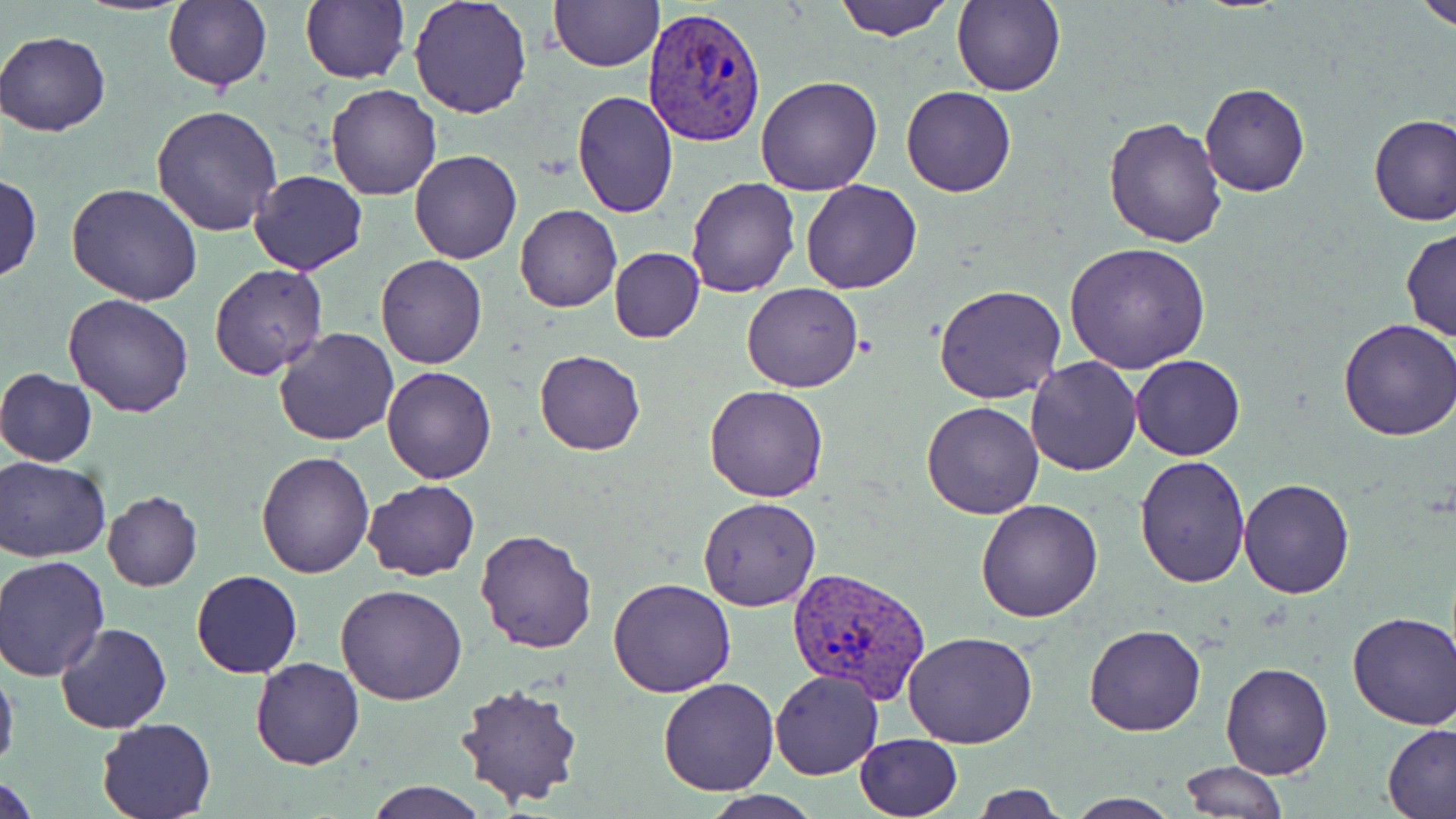

{
  "slide_level_diagnosis": "Plasmodium vivax",
  "stain": "May-Grünwald-Giemsa",
  "image_size": "1456×819 pixels",
  "field_of_view": "single",
  "preparation": "thin blood film",
  "plasmodium_vivax_infected_red_blood_cell_locations": "approximate bounding boxes as named x1/y1/x2/y2 corners in pixels: (x1=641, y1=6, x2=767, y2=149), (x1=788, y1=565, x2=931, y2=704)",
  "uninfected_red_blood_cell_locations": "approximate bounding boxes as named x1/y1/x2/y2 corners in pixels: (x1=74, y1=0, x2=194, y2=14), (x1=300, y1=0, x2=410, y2=84), (x1=407, y1=0, x2=533, y2=119), (x1=833, y1=0, x2=953, y2=42), (x1=952, y1=0, x2=1066, y2=98), (x1=1416, y1=0, x2=1456, y2=33), (x1=163, y1=1, x2=272, y2=92), (x1=548, y1=1, x2=662, y2=71), (x1=1, y1=29, x2=111, y2=137), (x1=755, y1=74, x2=883, y2=197), (x1=326, y1=83, x2=442, y2=201), (x1=1199, y1=83, x2=1311, y2=198), (x1=901, y1=87, x2=1017, y2=196), (x1=572, y1=90, x2=679, y2=217), (x1=149, y1=103, x2=283, y2=237), (x1=1367, y1=113, x2=1456, y2=227), (x1=1103, y1=115, x2=1229, y2=248), (x1=409, y1=148, x2=522, y2=265), (x1=248, y1=170, x2=368, y2=276), (x1=0, y1=173, x2=43, y2=283), (x1=684, y1=176, x2=800, y2=298), (x1=800, y1=178, x2=923, y2=294), (x1=66, y1=182, x2=203, y2=306), (x1=515, y1=205, x2=622, y2=312), (x1=1400, y1=228, x2=1455, y2=342), (x1=1064, y1=241, x2=1211, y2=374), (x1=609, y1=247, x2=705, y2=344), (x1=376, y1=255, x2=487, y2=369), (x1=208, y1=265, x2=329, y2=381), (x1=741, y1=280, x2=863, y2=393), (x1=935, y1=283, x2=1067, y2=405), (x1=63, y1=293, x2=194, y2=419), (x1=1334, y1=318, x2=1456, y2=440), (x1=273, y1=326, x2=401, y2=446), (x1=534, y1=349, x2=646, y2=455), (x1=1130, y1=354, x2=1244, y2=460), (x1=1026, y1=356, x2=1141, y2=475), (x1=382, y1=366, x2=497, y2=484), (x1=0, y1=368, x2=98, y2=466), (x1=705, y1=385, x2=829, y2=503), (x1=920, y1=401, x2=1046, y2=520), (x1=256, y1=450, x2=374, y2=578), (x1=0, y1=456, x2=110, y2=562), (x1=1134, y1=456, x2=1252, y2=589), (x1=1238, y1=478, x2=1355, y2=599), (x1=361, y1=480, x2=481, y2=580), (x1=102, y1=489, x2=202, y2=592), (x1=697, y1=496, x2=821, y2=611), (x1=976, y1=497, x2=1105, y2=622), (x1=474, y1=529, x2=596, y2=654), (x1=2, y1=556, x2=112, y2=681), (x1=190, y1=569, x2=302, y2=679), (x1=608, y1=577, x2=737, y2=697), (x1=335, y1=583, x2=468, y2=705), (x1=1346, y1=611, x2=1455, y2=729), (x1=56, y1=623, x2=171, y2=734), (x1=1084, y1=623, x2=1206, y2=737), (x1=902, y1=629, x2=1038, y2=749), (x1=250, y1=658, x2=364, y2=769), (x1=0, y1=659, x2=19, y2=778), (x1=1220, y1=662, x2=1333, y2=779), (x1=770, y1=670, x2=885, y2=780), (x1=657, y1=677, x2=780, y2=796), (x1=454, y1=681, x2=586, y2=811), (x1=95, y1=716, x2=219, y2=819), (x1=1383, y1=722, x2=1456, y2=817), (x1=855, y1=732, x2=962, y2=818), (x1=1177, y1=760, x2=1286, y2=817), (x1=2, y1=773, x2=39, y2=819), (x1=366, y1=781, x2=487, y2=819), (x1=966, y1=783, x2=1066, y2=817), (x1=698, y1=792, x2=826, y2=819), (x1=1064, y1=794, x2=1184, y2=819)",
  "modality": "optical microscopy",
  "magnification": "1000x"
}